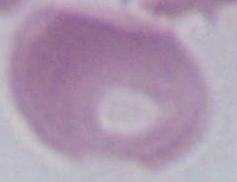

modality = photomicrograph
magnification = 1000x
identification = red blood cell